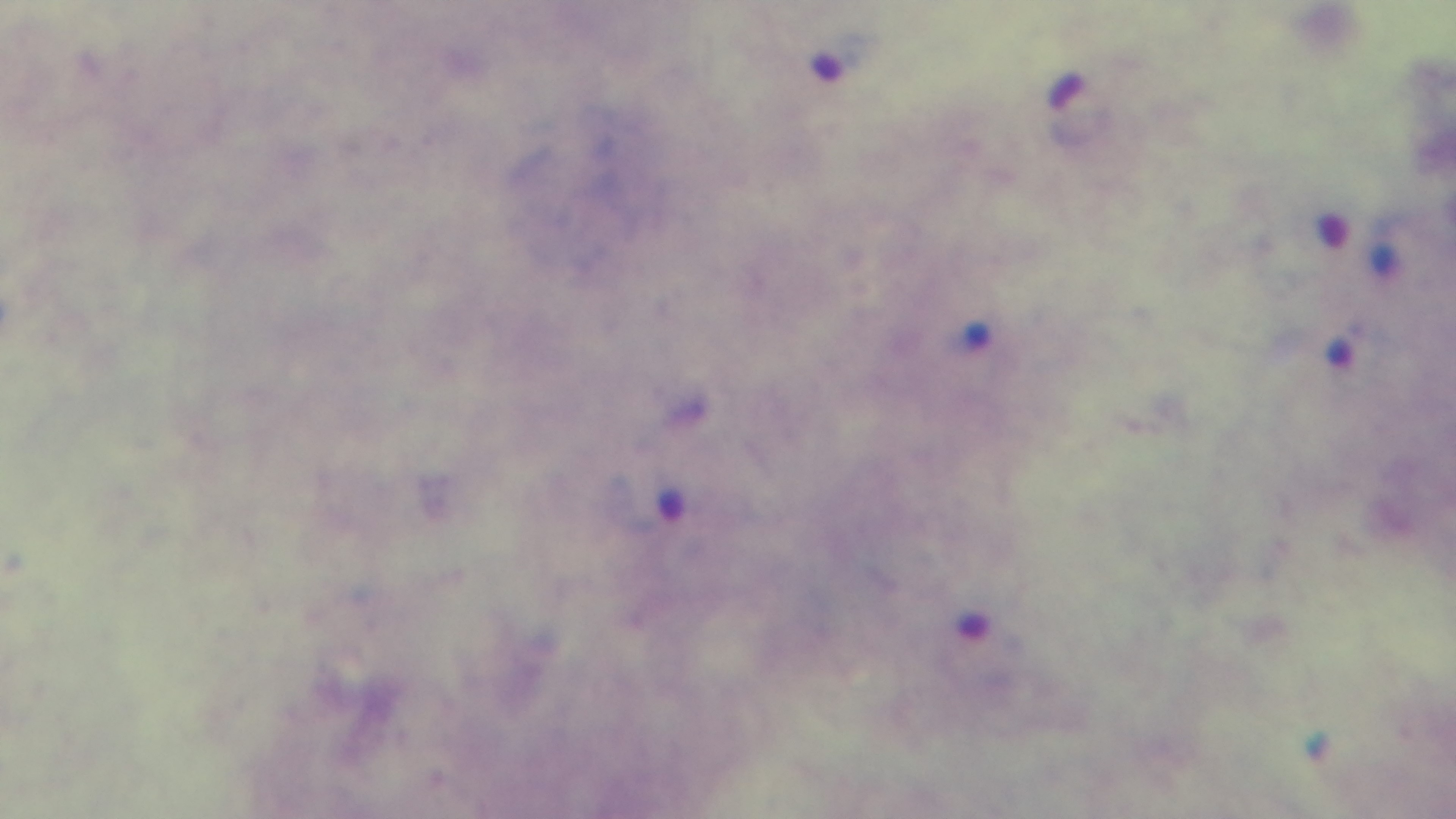
Summary:
  - Modality: light microscopy
  - Malaria status: positive
  - Capture: mounted 4K digital camera
  - Preparation: thick blood film
  - Objective: 100x oil immersion
  - Stain: Giemsa
  - Field of view: one from the slide